Identify the parasite.
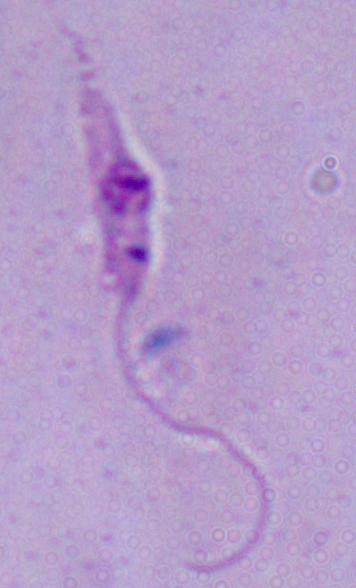

This is Leishmania.

magnification: 1000x
modality: photomicrograph